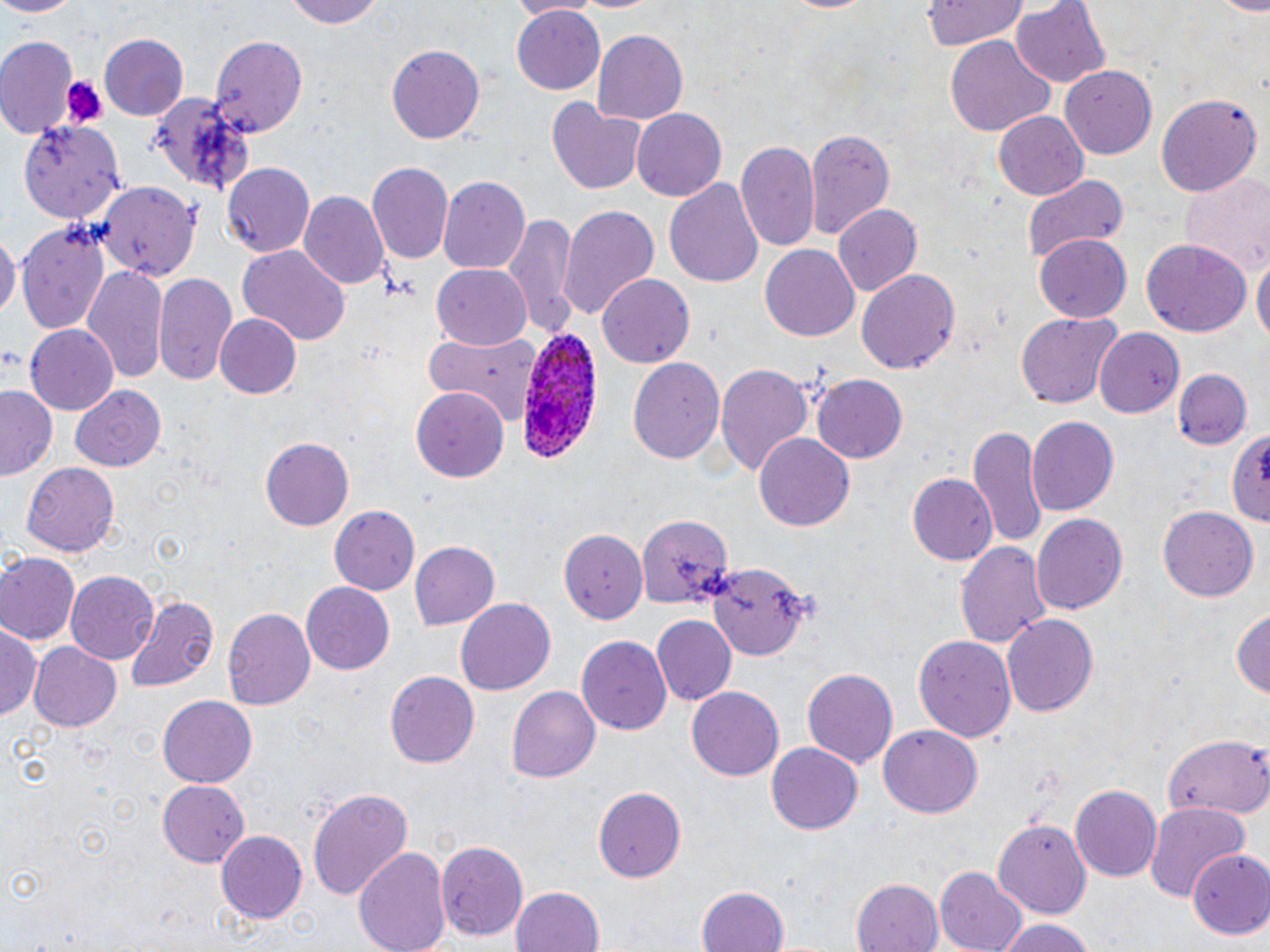

Approximate bounding boxes as [x1, y1, x2, y2] in pixels. Uninfected red blood cell locations: [0, 0, 80, 18], [280, 0, 385, 27], [506, 0, 597, 18], [924, 0, 1027, 50], [1012, 2, 1109, 89], [510, 9, 606, 98], [592, 30, 689, 126], [0, 34, 80, 140], [944, 34, 1055, 136], [100, 35, 187, 118], [210, 35, 308, 138], [387, 45, 486, 143], [1059, 66, 1158, 160], [143, 92, 255, 195], [1155, 92, 1262, 198], [547, 99, 647, 196], [632, 108, 726, 200], [993, 110, 1087, 202], [18, 121, 123, 223], [804, 128, 893, 238], [736, 141, 819, 256], [366, 161, 454, 264], [222, 164, 316, 256], [1022, 173, 1130, 267], [438, 175, 531, 274], [663, 177, 764, 290], [96, 183, 202, 279], [298, 192, 387, 289], [833, 203, 922, 296], [560, 204, 660, 321], [502, 214, 577, 340], [15, 221, 112, 336], [0, 232, 17, 324], [1034, 232, 1132, 323], [1140, 240, 1251, 337], [761, 243, 860, 341], [236, 247, 349, 349], [1253, 256, 1269, 347], [431, 265, 532, 348], [83, 267, 168, 384], [857, 269, 961, 376], [154, 271, 240, 388], [599, 273, 693, 367], [1015, 313, 1122, 408], [216, 314, 302, 398], [26, 325, 120, 414], [423, 327, 546, 425], [1093, 328, 1183, 421], [627, 356, 724, 468], [713, 361, 816, 476], [1172, 369, 1252, 450], [813, 375, 909, 462], [70, 384, 166, 471], [411, 385, 512, 481], [1, 386, 59, 481], [1026, 418, 1118, 516], [969, 424, 1048, 552], [1224, 428, 1270, 525], [754, 433, 853, 533], [262, 439, 354, 529], [20, 461, 120, 556], [909, 473, 1000, 566], [1157, 504, 1260, 602], [328, 506, 421, 597], [1030, 512, 1128, 615], [637, 516, 731, 609], [561, 527, 650, 623], [956, 539, 1052, 651], [409, 542, 499, 630], [0, 553, 79, 645], [709, 561, 808, 660], [66, 571, 158, 663], [301, 581, 395, 674], [124, 596, 217, 694], [453, 599, 556, 697], [1233, 601, 1269, 699], [224, 608, 316, 712], [1001, 614, 1098, 717], [650, 615, 735, 706], [0, 627, 42, 721], [914, 633, 1015, 742], [576, 638, 671, 734], [28, 642, 122, 732], [801, 667, 897, 770], [385, 669, 480, 768], [508, 686, 600, 783], [686, 686, 785, 780], [157, 694, 257, 787], [878, 726, 980, 818], [1158, 730, 1270, 817], [767, 743, 863, 834], [157, 780, 252, 867], [1071, 784, 1162, 881], [307, 787, 412, 901], [594, 787, 687, 881], [1145, 802, 1249, 903], [994, 819, 1091, 922], [216, 830, 307, 925], [435, 838, 529, 941], [354, 843, 453, 952], [1186, 850, 1269, 939], [935, 867, 1028, 952], [853, 876, 943, 952], [511, 885, 606, 952], [697, 888, 787, 952], [993, 918, 1099, 952]. Plasmodium ovale-infected red blood cell locations: [517, 324, 605, 464]. Platelet locations: [63, 76, 105, 125]. Slide-level diagnosis: Plasmodium ovale. Captured at 1000x magnification. May-Grünwald-Giemsa stain. Optical microscopy. Image is 1270×952 pixels. Thin blood film. One field of a larger specimen.